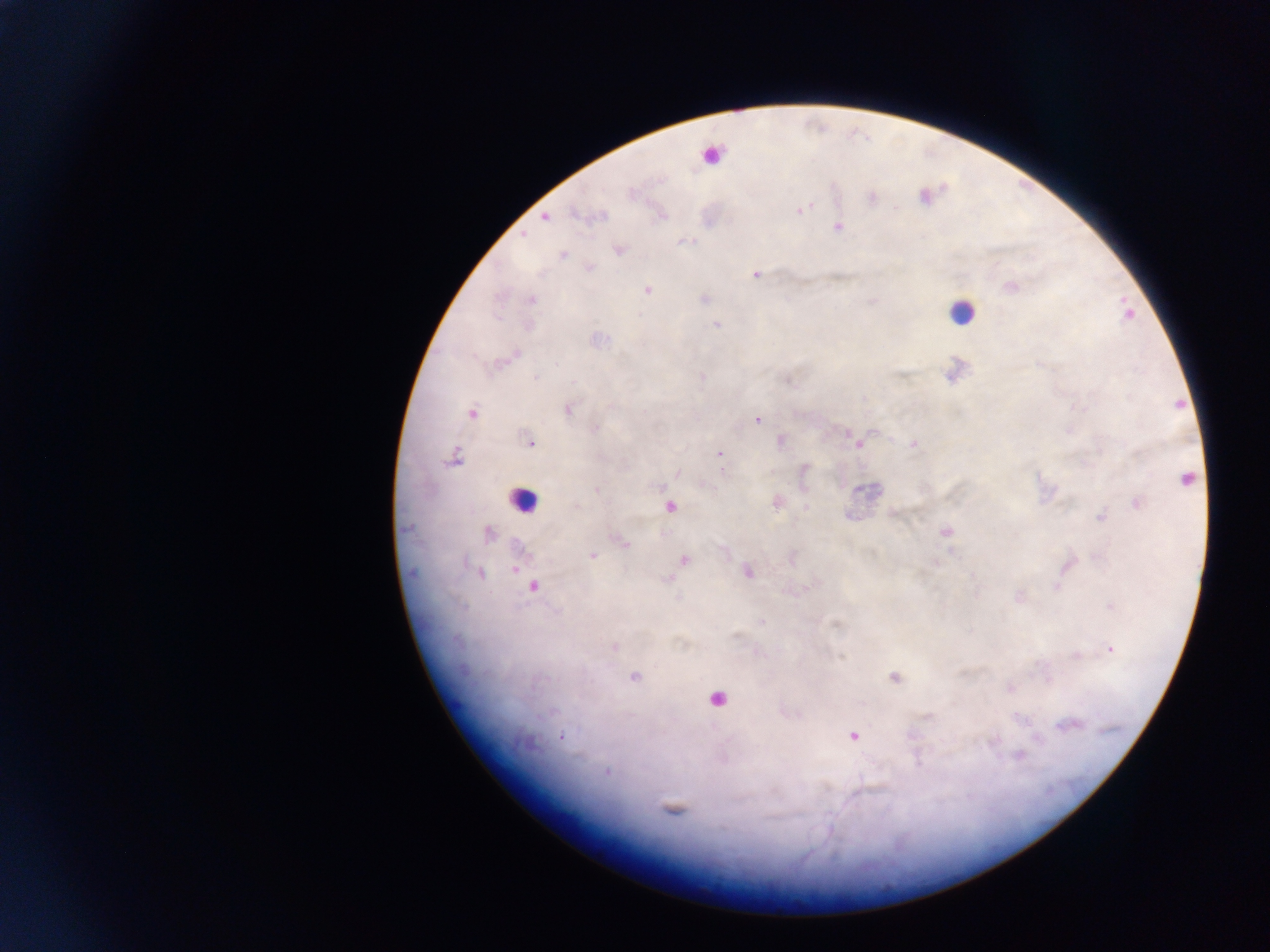

Approximate centers as (x, y) in pixels.
Summary:
  - Plasmodium parasite locations: (632, 193), (924, 195), (870, 197), (799, 209), (597, 216), (545, 217), (838, 226), (685, 241), (617, 249), (562, 254), (588, 267), (756, 273), (1011, 286), (647, 289), (703, 298), (531, 299), (717, 324), (954, 370), (701, 376), (566, 408), (472, 414), (757, 420), (780, 441), (529, 443), (859, 443), (914, 443), (719, 454), (453, 458), (803, 470), (1187, 479), (597, 489), (866, 491), (775, 501), (1137, 501), (670, 506), (893, 514), (1101, 517), (406, 529), (945, 532), (488, 533), (622, 542), (592, 555), (791, 557), (683, 559), (516, 565), (1068, 565), (746, 572), (479, 574), (973, 576), (667, 578), (533, 586), (1018, 596), (1111, 606), (762, 622), (614, 646), (1109, 648), (1075, 655), (633, 676), (893, 677), (1010, 687), (1070, 724), (853, 735), (560, 737), (1018, 754), (606, 771), (671, 809)
  - Leukocyte locations: (710, 153), (961, 312), (522, 500), (715, 699)
  - Field of view: single
  - Country: Ghana
  - Preparation: thick blood smear
  - Image size: 1270×952 pixels
  - Capture: mobile-phone photograph through a microscope